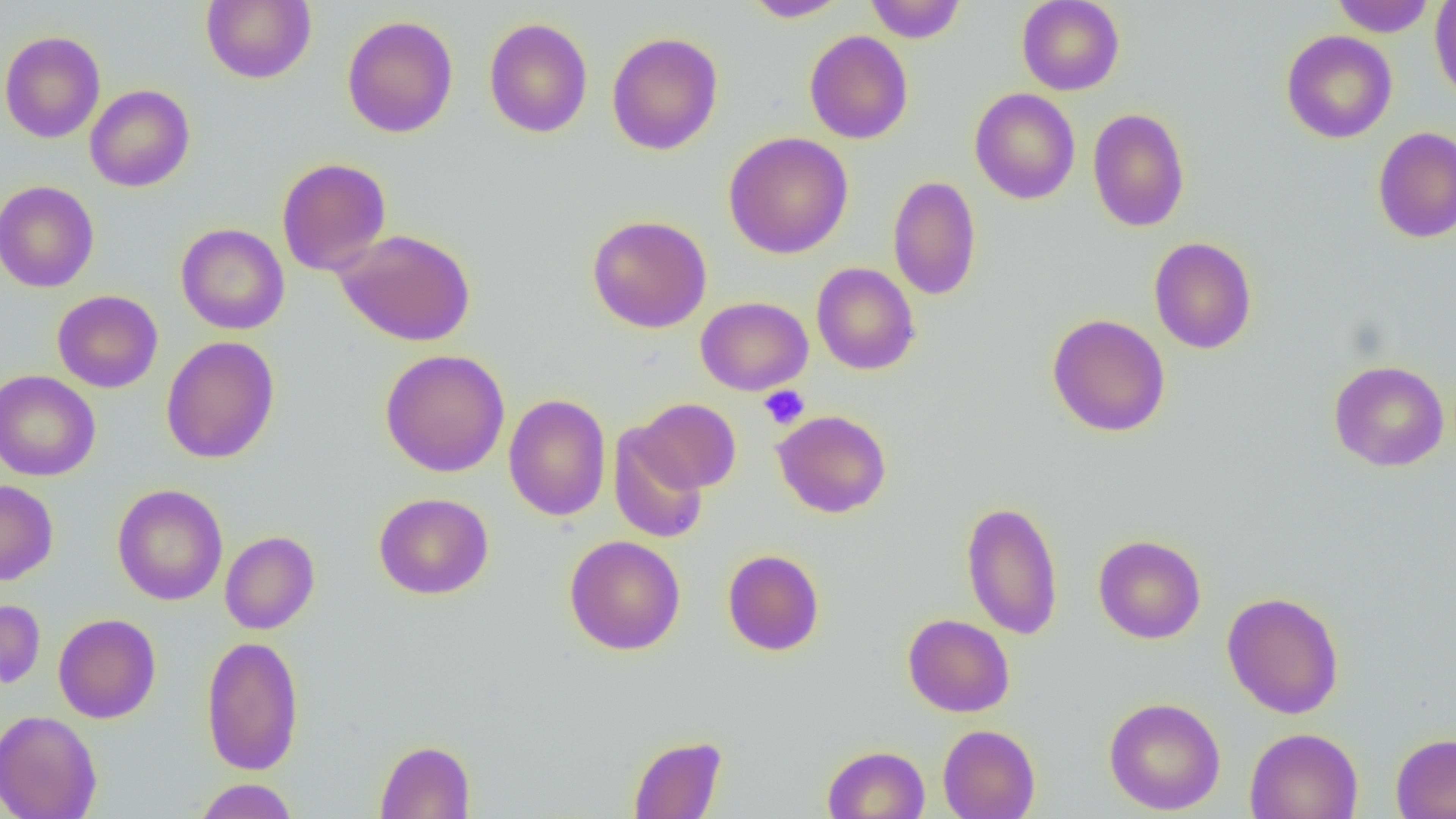

Summary:
  - Coordinate format: approximate bounding boxes as (x1, y1, x2, y2) in pixels
  - Uninfected red blood cell locations: (201, 0, 317, 84), (745, 0, 849, 22), (865, 0, 966, 42), (1016, 0, 1124, 95), (1330, 0, 1436, 36), (1429, 0, 1456, 104), (342, 15, 458, 138), (483, 17, 593, 138), (0, 30, 106, 143), (804, 30, 913, 144), (1280, 30, 1398, 143), (606, 31, 724, 155), (85, 85, 195, 192), (969, 87, 1081, 204), (1088, 107, 1190, 232), (1372, 126, 1456, 243), (724, 132, 853, 259), (277, 158, 391, 276), (888, 175, 982, 301), (0, 180, 100, 293), (587, 214, 713, 333), (176, 223, 290, 334), (334, 228, 476, 347), (1149, 237, 1257, 354), (811, 263, 921, 375), (52, 290, 163, 393), (696, 296, 813, 395), (1047, 313, 1171, 436), (161, 336, 280, 464), (380, 349, 510, 477), (1327, 359, 1450, 472), (0, 370, 101, 481), (503, 394, 611, 521), (633, 398, 741, 494), (772, 410, 892, 518), (608, 426, 709, 543), (0, 479, 58, 586), (112, 484, 228, 606), (373, 492, 494, 599), (961, 499, 1063, 640), (220, 530, 320, 634), (1093, 534, 1206, 644), (564, 535, 685, 655), (722, 549, 825, 656), (1222, 591, 1345, 719), (0, 599, 45, 689), (53, 613, 161, 723), (902, 614, 1015, 717), (201, 635, 305, 776), (1103, 696, 1226, 815), (0, 709, 102, 819), (938, 724, 1041, 819), (1244, 727, 1363, 819), (1390, 732, 1456, 818), (628, 735, 728, 818), (374, 739, 476, 818), (822, 745, 930, 819), (193, 778, 298, 819)
  - Platelet locations: (759, 385, 810, 430)
  - Slide-level diagnosis: negative for blood parasites
  - Preparation: thin blood film
  - Magnification: 1000x
  - Modality: light microscopy
  - Field of view: single
  - Image size: 1456×819 pixels